Assess this cell for malaria.
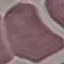
It is uninfected.

Summary:
  - Stain: Giemsa
  - Capture: smartphone through the microscope eyepiece
  - Image type: automatically extracted cell patch, resized to 64 × 64 pixels
  - Preparation: thin blood film